Classify this cell by malaria status.
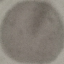

It is uninfected.

Photographed with a smartphone camera at the microscope eyepiece. Giemsa-stained preparation. Cell patch, automatically extracted from a larger field of view and resized to 64 × 64 pixels. Thin blood film.